Outline platelets.
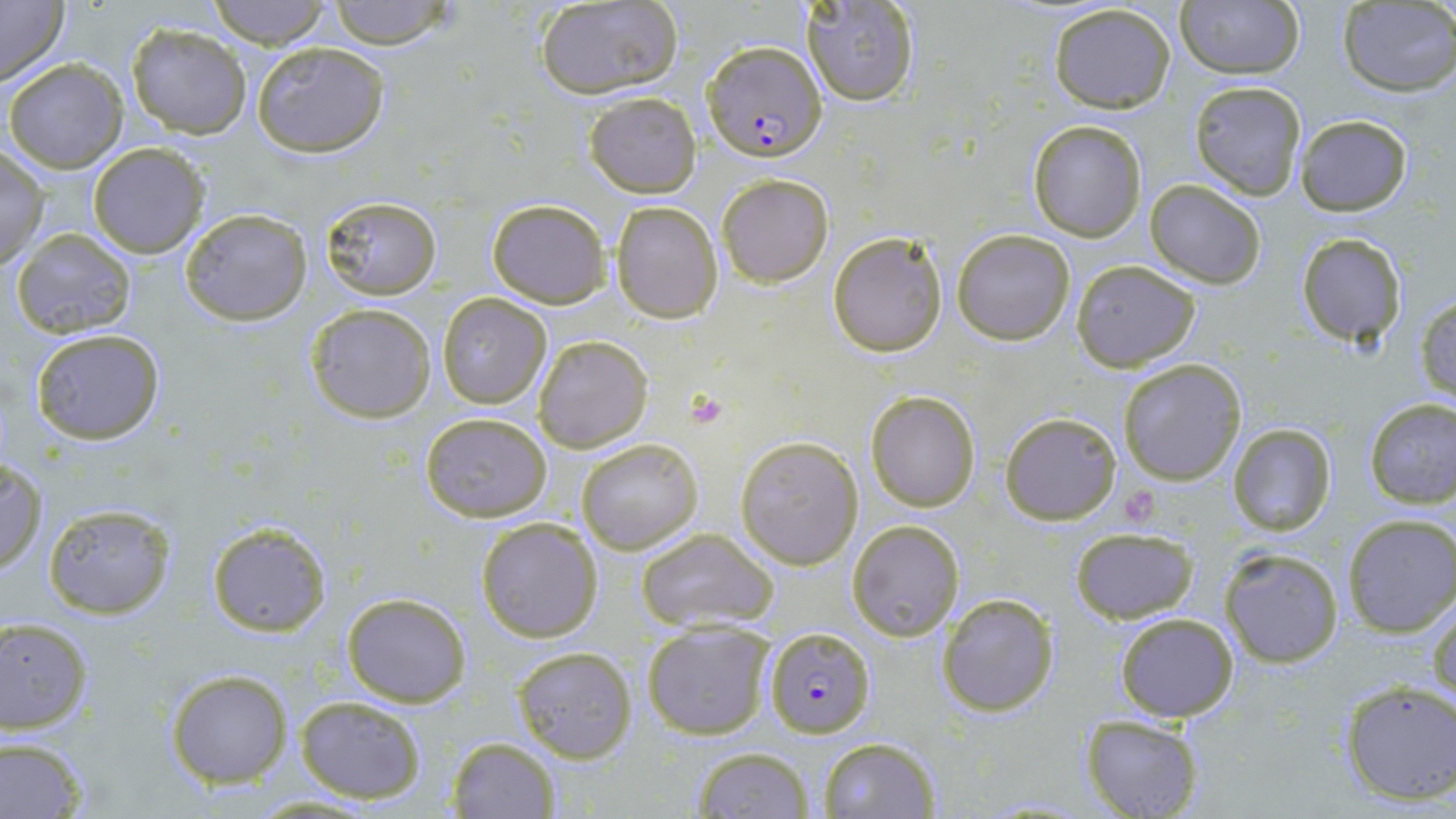

Approximate bounding boxes as (x1, y1, x2, y2) in pixels.
Platelets: (683, 389, 734, 432), (1118, 486, 1163, 528).

slide-level diagnosis = Plasmodium falciparum
stain = May-Grünwald-Giemsa
magnification = 1000x
Plasmodium falciparum-infected red blood cell locations = approximate bounding boxes as (x1, y1, x2, y2) in pixels: (702, 41, 830, 163), (763, 628, 874, 738)
modality = optical microscopy
field of view = one of a larger specimen
uninfected red blood cell locations = approximate bounding boxes as (x1, y1, x2, y2) in pixels: (0, 0, 70, 87), (208, 0, 331, 47), (324, 0, 459, 49), (1176, 0, 1306, 80), (800, 1, 920, 106), (533, 2, 684, 100), (1337, 3, 1456, 95), (1047, 4, 1177, 113), (125, 23, 253, 137), (251, 42, 389, 159), (4, 57, 128, 172), (1188, 80, 1306, 200), (582, 92, 701, 198), (1293, 113, 1414, 216), (1027, 118, 1147, 242), (87, 142, 211, 259), (0, 148, 48, 270), (717, 173, 833, 287), (1145, 179, 1268, 289), (321, 197, 442, 299), (487, 198, 609, 308), (610, 202, 723, 323), (179, 207, 312, 326), (952, 227, 1076, 345), (12, 229, 137, 339), (827, 232, 949, 356), (1294, 233, 1408, 348), (1070, 260, 1203, 369), (1415, 292, 1456, 403), (437, 293, 552, 408), (305, 302, 437, 423), (28, 327, 165, 446), (532, 334, 653, 453), (1118, 357, 1248, 485), (866, 390, 980, 512), (1364, 397, 1456, 508), (419, 412, 553, 522), (1000, 412, 1121, 525), (1226, 424, 1336, 535), (574, 436, 705, 555), (735, 436, 865, 570), (1, 457, 48, 576), (44, 504, 175, 618), (1341, 514, 1456, 637), (475, 516, 605, 643), (846, 517, 966, 642), (205, 522, 331, 637), (1069, 527, 1198, 624), (635, 528, 781, 635), (1218, 546, 1344, 668), (938, 591, 1059, 716), (340, 592, 471, 708), (1429, 598, 1455, 709), (1115, 611, 1239, 720), (0, 616, 94, 735), (642, 621, 775, 740), (510, 645, 639, 764), (164, 669, 293, 788), (1338, 680, 1456, 806), (295, 695, 428, 804), (1081, 714, 1205, 819), (817, 735, 941, 819), (445, 736, 559, 818), (0, 737, 91, 817), (690, 745, 813, 818)
image size = 1456×819 pixels
preparation = thin blood smear